Assess this cell for malaria.
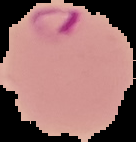

Parasitized.

Summary:
  - Image type: cell region segmented out of the field of view; surrounding area masked to black
  - Preparation: thin blood smear
  - Image size: 136×142 pixels